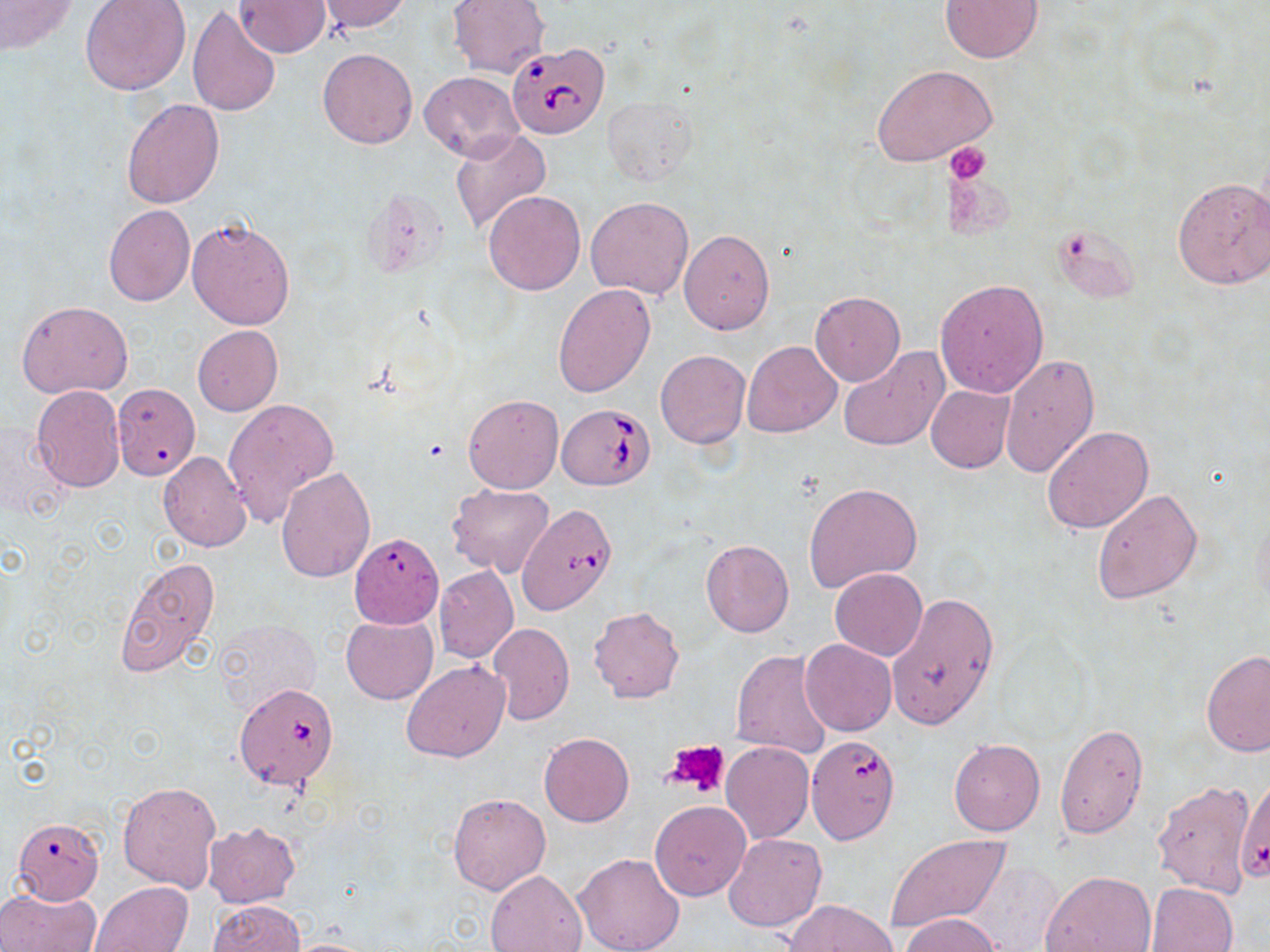

slide_level_diagnosis: Babesia divergens
platelet_locations: 'approximate bounding boxes as named x1/y1/x2/y2 corners in pixels: (x1=947, y1=142, x2=991, y2=184), (x1=663, y1=739, x2=732, y2=799)'
image_size: 1270×952 pixels
preparation: thin blood smear
modality: light microscopy
uninfected_red_blood_cell_locations: 'approximate bounding boxes as named x1/y1/x2/y2 corners in pixels: (x1=0, y1=0, x2=76, y2=54), (x1=232, y1=0, x2=331, y2=57), (x1=315, y1=0, x2=411, y2=34), (x1=447, y1=0, x2=550, y2=78), (x1=940, y1=0, x2=1043, y2=63), (x1=79, y1=1, x2=190, y2=95), (x1=187, y1=6, x2=280, y2=117), (x1=318, y1=48, x2=416, y2=148), (x1=873, y1=65, x2=996, y2=167), (x1=419, y1=71, x2=523, y2=163), (x1=120, y1=97, x2=224, y2=208), (x1=604, y1=98, x2=696, y2=185), (x1=449, y1=128, x2=552, y2=236), (x1=1171, y1=175, x2=1270, y2=290), (x1=484, y1=191, x2=586, y2=295), (x1=585, y1=197, x2=694, y2=299), (x1=103, y1=205, x2=195, y2=308), (x1=187, y1=217, x2=295, y2=330), (x1=679, y1=229, x2=775, y2=334), (x1=934, y1=279, x2=1049, y2=398), (x1=552, y1=282, x2=655, y2=399), (x1=809, y1=292, x2=905, y2=385), (x1=16, y1=300, x2=132, y2=398), (x1=192, y1=325, x2=282, y2=416), (x1=741, y1=340, x2=841, y2=438), (x1=838, y1=345, x2=949, y2=451), (x1=655, y1=350, x2=750, y2=448), (x1=998, y1=354, x2=1100, y2=478), (x1=113, y1=382, x2=204, y2=483), (x1=925, y1=384, x2=1015, y2=473), (x1=31, y1=385, x2=127, y2=493), (x1=463, y1=393, x2=563, y2=493), (x1=222, y1=398, x2=338, y2=524), (x1=0, y1=425, x2=69, y2=522), (x1=1041, y1=425, x2=1155, y2=534), (x1=158, y1=452, x2=253, y2=552), (x1=275, y1=467, x2=375, y2=583), (x1=804, y1=480, x2=923, y2=594), (x1=446, y1=483, x2=554, y2=578), (x1=1091, y1=487, x2=1204, y2=605), (x1=520, y1=507, x2=617, y2=621), (x1=336, y1=530, x2=445, y2=637), (x1=700, y1=539, x2=794, y2=638), (x1=114, y1=556, x2=221, y2=677), (x1=433, y1=566, x2=518, y2=663), (x1=829, y1=568, x2=928, y2=661), (x1=833, y1=571, x2=986, y2=695), (x1=887, y1=591, x2=1000, y2=732), (x1=589, y1=606, x2=684, y2=703), (x1=341, y1=614, x2=437, y2=704), (x1=213, y1=618, x2=322, y2=717), (x1=488, y1=622, x2=574, y2=725), (x1=800, y1=639, x2=897, y2=735), (x1=1201, y1=649, x2=1269, y2=758), (x1=732, y1=650, x2=834, y2=759), (x1=401, y1=661, x2=511, y2=761), (x1=1054, y1=723, x2=1149, y2=839), (x1=539, y1=732, x2=634, y2=827), (x1=948, y1=739, x2=1045, y2=836), (x1=721, y1=741, x2=814, y2=843), (x1=1236, y1=777, x2=1270, y2=885), (x1=1152, y1=779, x2=1257, y2=899), (x1=118, y1=780, x2=221, y2=893), (x1=449, y1=793, x2=551, y2=894), (x1=650, y1=801, x2=751, y2=902), (x1=11, y1=818, x2=105, y2=904), (x1=202, y1=822, x2=300, y2=909), (x1=724, y1=832, x2=825, y2=932), (x1=884, y1=835, x2=1010, y2=935), (x1=573, y1=851, x2=685, y2=952), (x1=485, y1=869, x2=587, y2=952), (x1=1040, y1=871, x2=1157, y2=952), (x1=90, y1=881, x2=192, y2=952), (x1=1145, y1=882, x2=1239, y2=952), (x1=1, y1=887, x2=100, y2=952), (x1=783, y1=899, x2=896, y2=951), (x1=207, y1=901, x2=306, y2=951), (x1=899, y1=912, x2=1002, y2=952), (x1=284, y1=937, x2=383, y2=952)'
field_of_view: one of a larger specimen
babesia_divergens_infected_red_blood_cell_locations: 'approximate bounding boxes as named x1/y1/x2/y2 corners in pixels: (x1=506, y1=42, x2=610, y2=139), (x1=558, y1=403, x2=656, y2=490), (x1=234, y1=682, x2=339, y2=790), (x1=805, y1=733, x2=900, y2=846)'
stain: May-Grünwald-Giemsa
magnification: 1000x